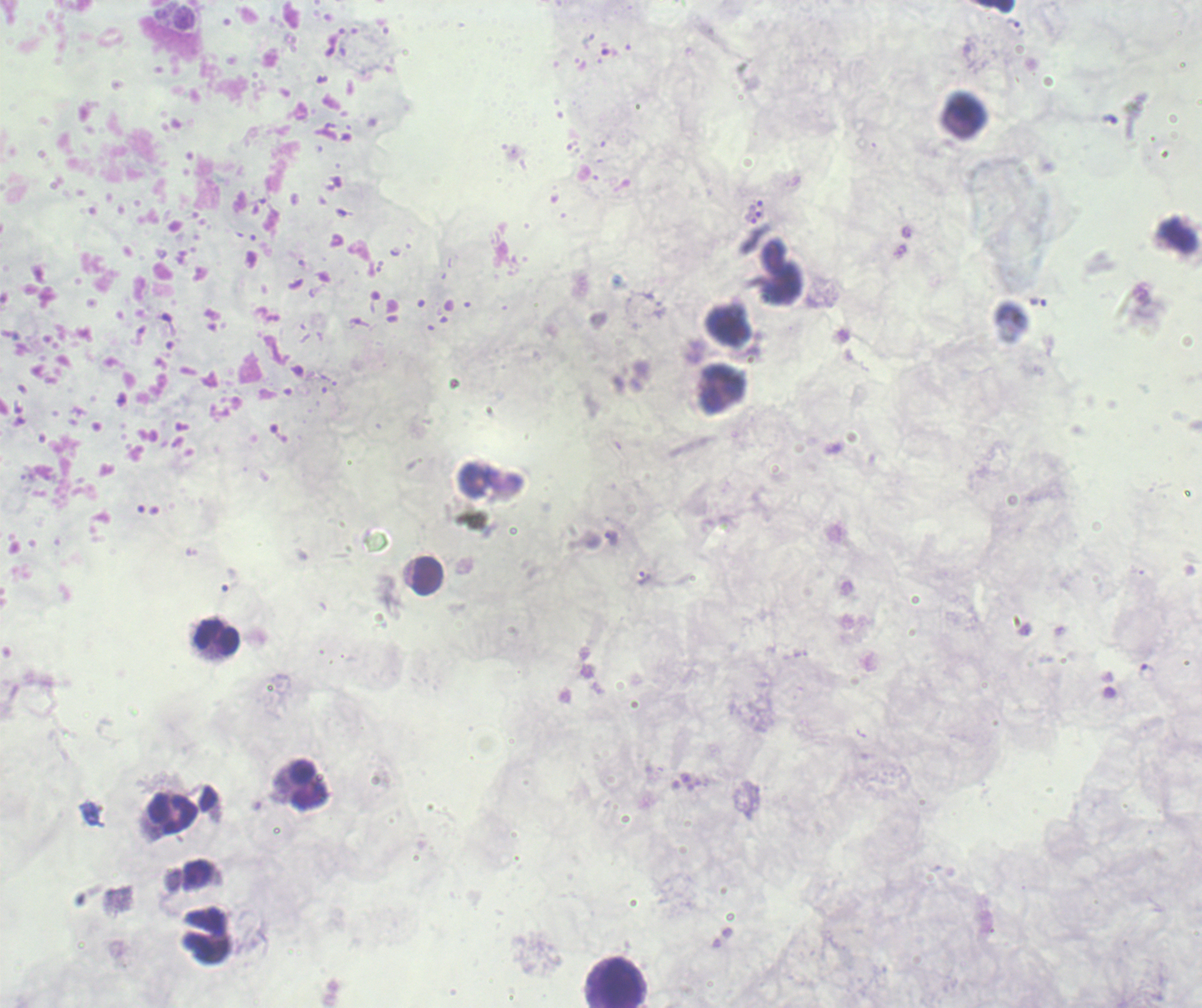

Approximate centers as (x, y) in pixels.
Summary:
  - Leukocyte locations: (966, 110), (722, 389), (427, 575), (217, 638), (308, 785), (173, 813), (620, 984)
  - Trophozoite locations: (1014, 23), (756, 206), (611, 538), (644, 578)
  - Background quality: unsatisfactory
  - Image size: 1202×1008 pixels
  - Context: previously used in a real diagnosis
  - Preparation: thick smear of blood
  - Stain: Romanowsky
  - Result: malaria parasites identified
  - Field of view: one from this slide
  - Magnification: 100x